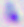

identification: Toxoplasma gondii
modality: micrograph
magnification: 400x